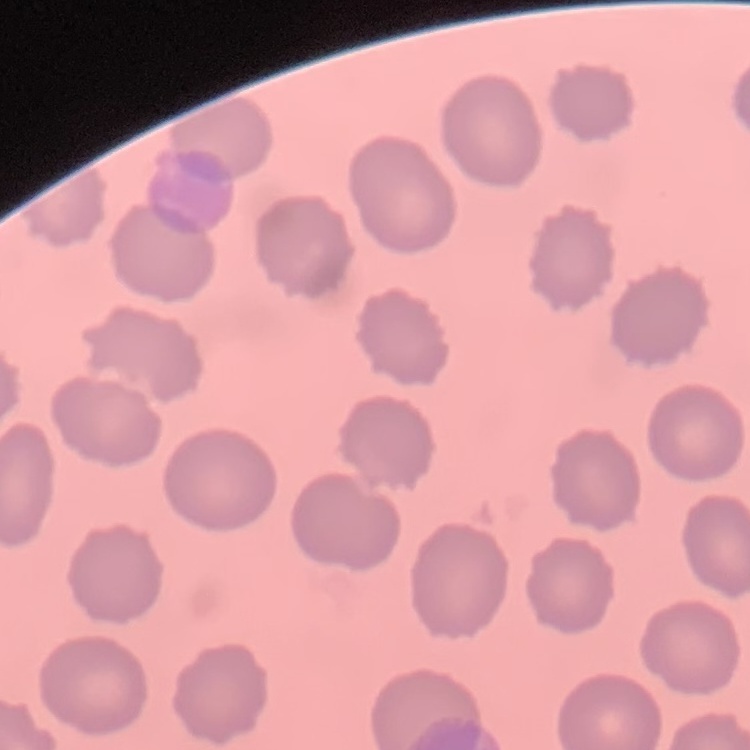 The erythrocytes exhibit no rouleaux formation. Stained with either Field's or Giemsa. Thin blood smear. Square crop of a larger photomicrograph.